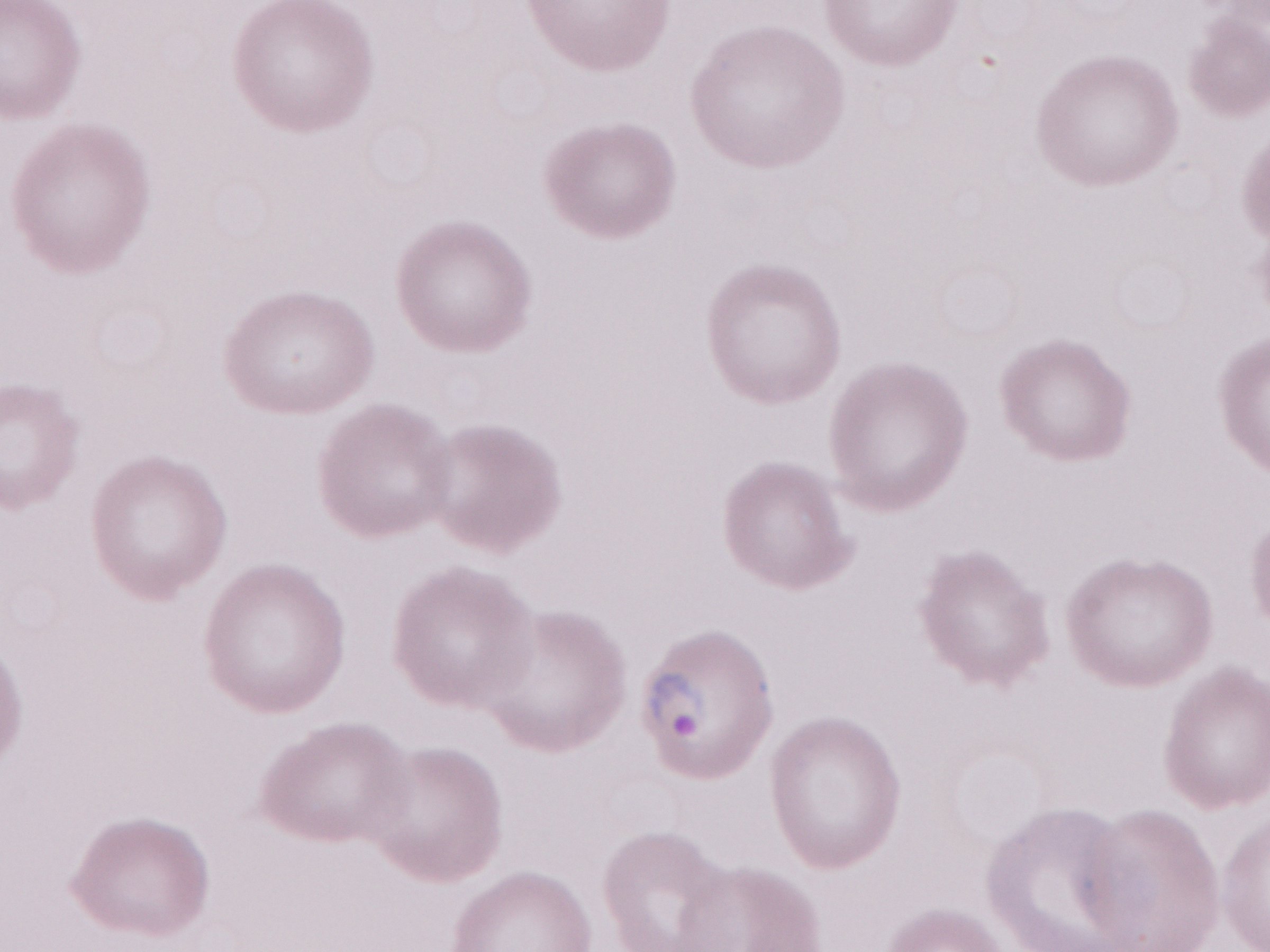

Image is 1270×952 pixels. 1,000x magnification. Thin blood film. Single field of view. Olympus BX43 microscope, Olympus DP73 camera. May-Grünwald-Giemsa stain. Patient diagnosis: malaria infection.